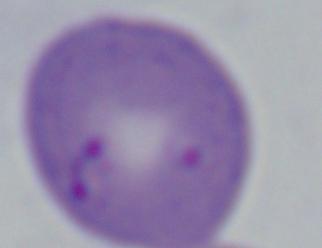
magnification = 1000x
modality = photomicrograph
identification = Babesia